Assess the morphology of the red blood cells.
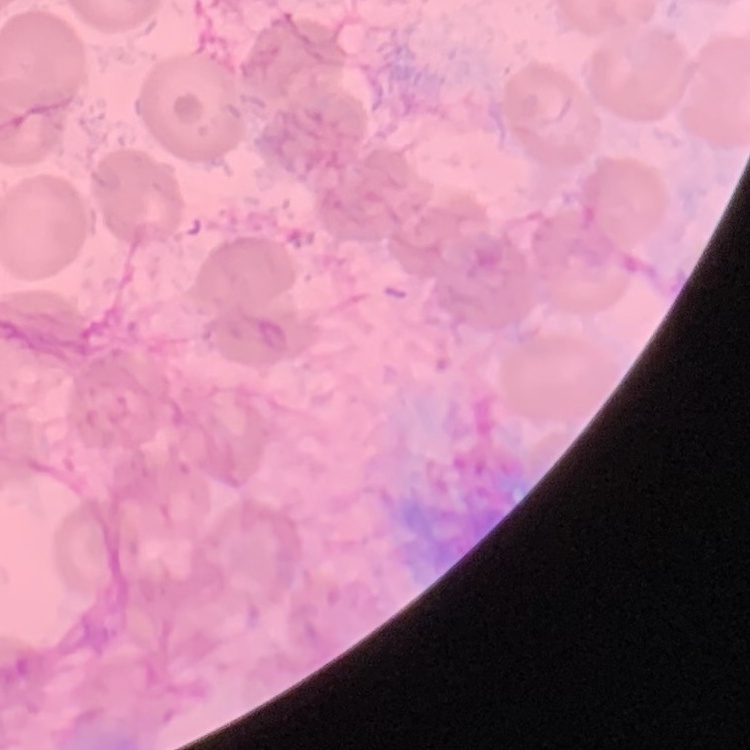
No rouleaux formation.

Field's or Giemsa stain. Square crop of a larger photomicrograph. Thin peripheral smear.